Classify this cell by malaria status.
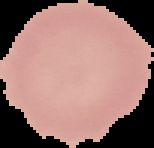

It is uninfected.

image size = 154×148 pixels
preparation = thin blood smear
image type = segmented cell region with the area outside set to black